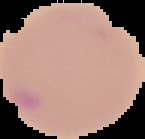

Summary:
  - Malaria status: parasitized
  - Preparation: thin blood smear
  - Image type: segmented cell region on a black background
  - Image size: 145×139 pixels